Point out each Plasmodium parasite.
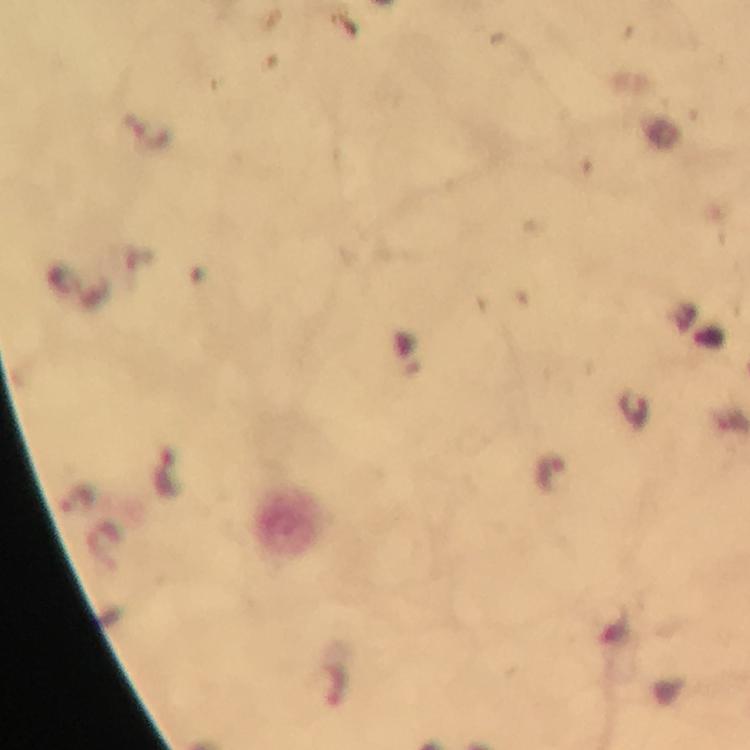

Approximate centers as (x, y) in pixels.
Plasmodium parasites: (331, 684).

Summary:
  - Capture: smartphone camera through the microscope
  - Cropped from: a single field of view
  - Immersion oil: used
  - Stain: Giemsa
  - Preparation: thick blood smear
  - Image size: 750×750 pixels
  - Magnification: 100x
  - Context: from a malaria diagnostic workup